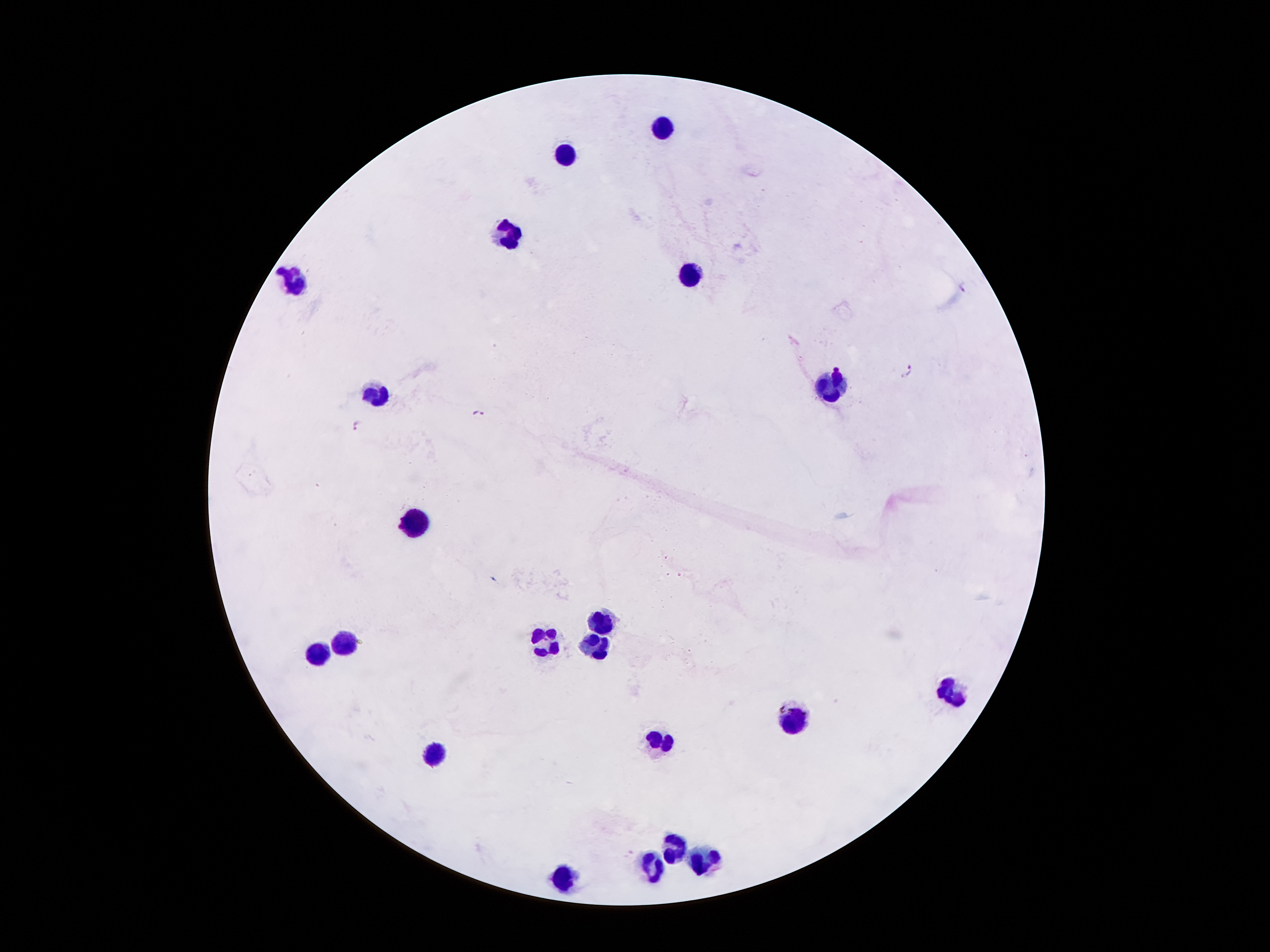
Approximate object centers, in pixels from the top-left corner.
Summary:
  - Leukocyte locations: (x=668, y=129), (x=565, y=156), (x=510, y=242), (x=691, y=278), (x=294, y=280), (x=832, y=389), (x=376, y=391), (x=416, y=523), (x=607, y=618), (x=347, y=643), (x=540, y=643), (x=599, y=647), (x=315, y=651), (x=954, y=689), (x=792, y=721), (x=659, y=742), (x=433, y=754), (x=674, y=840), (x=704, y=857), (x=653, y=872), (x=569, y=878)
  - Malaria parasite locations: (x=909, y=370), (x=476, y=413), (x=358, y=424)
  - Magnification: 100x
  - Patient malaria status: infected with Plasmodium falciparum
  - Stain: Giemsa
  - Image size: 1270×952 pixels
  - Preparation: thick peripheral-blood smear
  - Capture: smartphone through the microscope eyepiece
  - Field of view: one from this slide